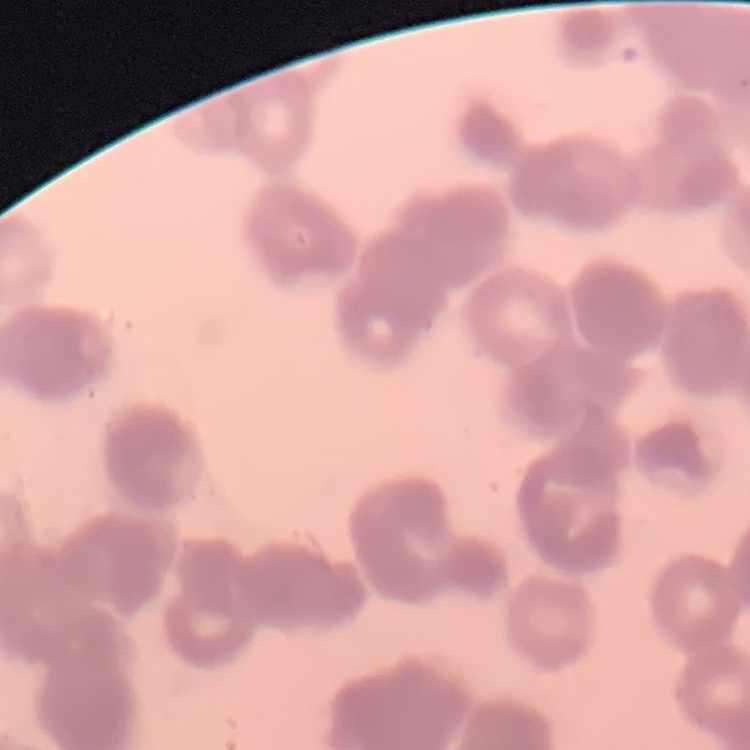
erythrocyte morphology = rouleaux formation
preparation = thin peripheral smear
stain = Field's or Giemsa
image type = square crop of a larger photomicrograph